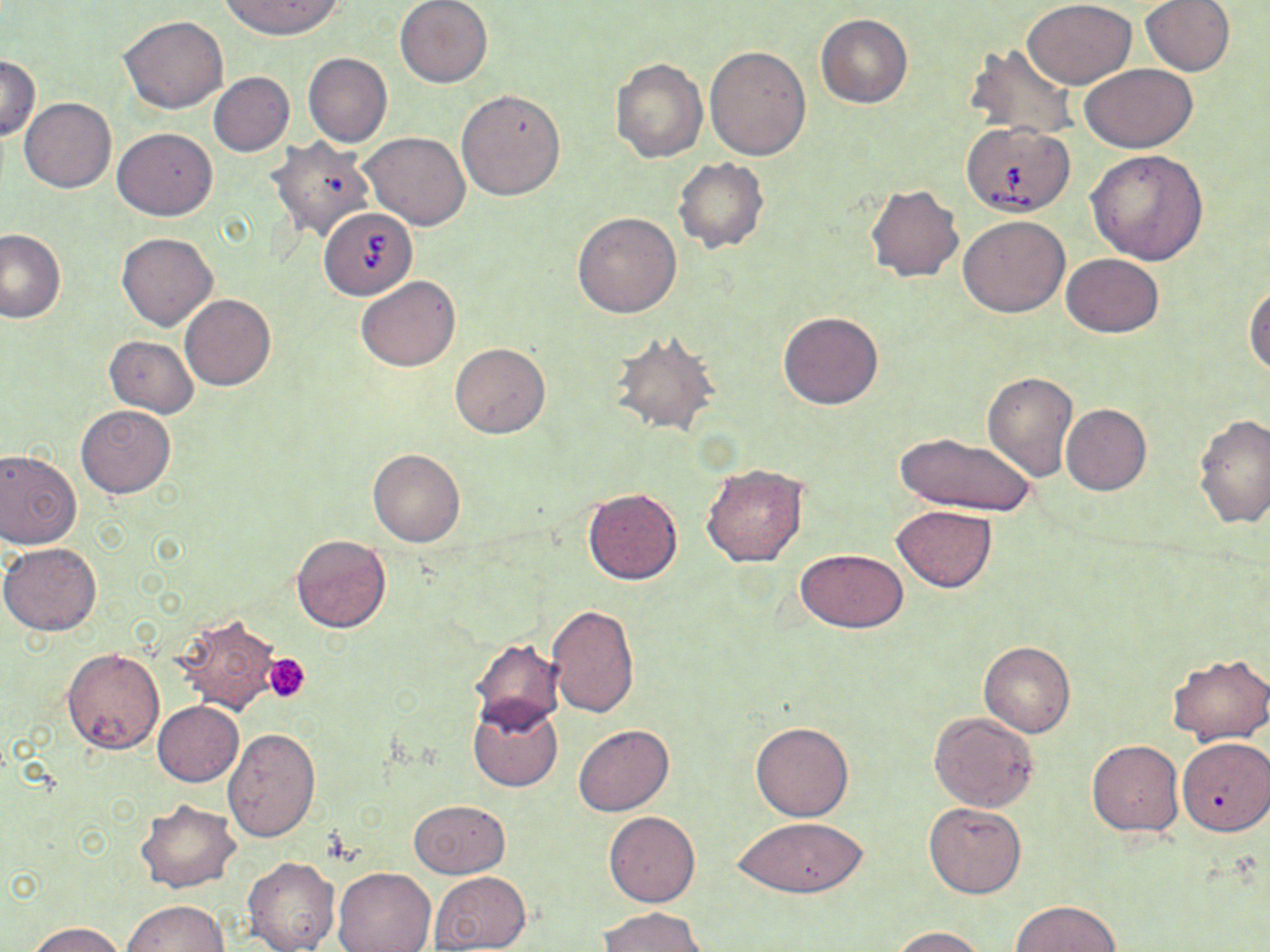

slide_level_diagnosis: Babesia divergens
field_of_view: single
uninfected_red_blood_cell_locations: 'approximate bounding boxes as (x1, y1, x2, y2) in pixels: (219, 0, 344, 39), (394, 0, 493, 87), (1022, 0, 1137, 88), (1140, 0, 1235, 75), (815, 13, 913, 108), (118, 15, 228, 113), (965, 44, 1079, 139), (704, 45, 811, 160), (303, 53, 392, 147), (0, 55, 41, 142), (610, 57, 708, 162), (1081, 64, 1198, 151), (209, 73, 294, 156), (457, 89, 565, 200), (20, 98, 115, 192), (112, 128, 217, 219), (360, 132, 470, 230), (267, 137, 375, 241), (1087, 149, 1209, 264), (673, 157, 769, 253), (865, 183, 964, 283), (573, 211, 682, 317), (958, 215, 1070, 317), (0, 228, 65, 322), (117, 232, 217, 330), (1060, 254, 1165, 338), (356, 274, 460, 371), (1244, 281, 1270, 375), (181, 294, 275, 390), (778, 311, 884, 409), (607, 333, 721, 437), (105, 336, 198, 417), (450, 342, 550, 439), (982, 372, 1078, 480), (75, 404, 176, 497), (1061, 404, 1152, 494), (1193, 413, 1270, 529), (895, 431, 1037, 516), (368, 448, 465, 546), (0, 449, 81, 549), (701, 462, 809, 567), (582, 488, 682, 584), (892, 505, 996, 592), (290, 534, 392, 633), (1, 542, 102, 637), (796, 550, 908, 631), (547, 603, 641, 718), (171, 614, 280, 714), (468, 638, 564, 732), (980, 642, 1075, 737), (63, 648, 164, 753), (1167, 652, 1270, 745), (468, 699, 563, 791), (152, 701, 243, 786), (930, 713, 1039, 810), (751, 721, 854, 821), (573, 724, 674, 816), (223, 727, 321, 842), (1176, 738, 1270, 835), (1086, 740, 1184, 836), (410, 799, 510, 878), (134, 800, 240, 892), (923, 803, 1025, 898), (604, 811, 700, 907), (735, 817, 867, 897), (242, 855, 340, 952), (332, 866, 438, 952), (429, 870, 532, 952), (121, 900, 230, 951), (1011, 900, 1121, 951), (600, 906, 707, 951), (28, 921, 126, 952), (891, 927, 989, 952)'
platelet_locations: 'approximate bounding boxes as (x1, y1, x2, y2) in pixels: (264, 653, 312, 701)'
preparation: thin blood film
magnification: 1000x
stain: May-Grünwald-Giemsa
modality: light microscopy
babesia_divergens_infected_red_blood_cell_locations: 'approximate bounding boxes as (x1, y1, x2, y2) in pixels: (961, 121, 1075, 214), (320, 207, 417, 299)'
image_size: 1270×952 pixels